Classify this cell by malaria status.
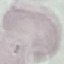
It is uninfected.

Summary:
  - Preparation: thin blood film
  - Capture: smartphone camera at the microscope eyepiece
  - Stain: Giemsa
  - Image type: cell patch, automatically extracted from a larger field of view and resized to 64 × 64 pixels